Assess this cell for malaria.
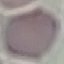

Uninfected.

Summary:
  - Capture: smartphone through the microscope eyepiece
  - Preparation: thin smear
  - Stain: Giemsa
  - Image type: automatically extracted cell patch, resized to 64 × 64 pixels